Name the parasite shown.
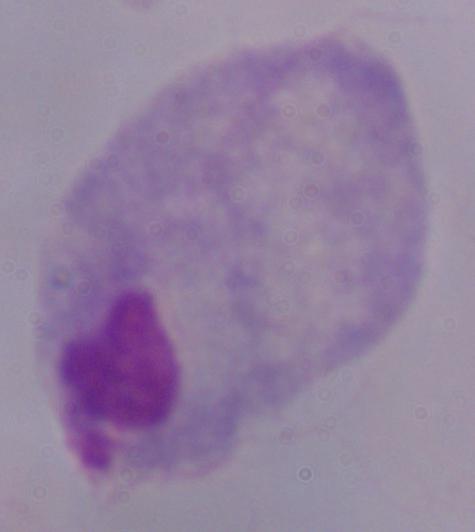

A trichomonad.

Photomicrograph. Captured at 1000x magnification.